Name the cell type shown.
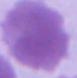

An erythrocyte.

Summary:
  - Modality: photomicrograph
  - Magnification: 1000x